Locate every uninfected red blood cell.
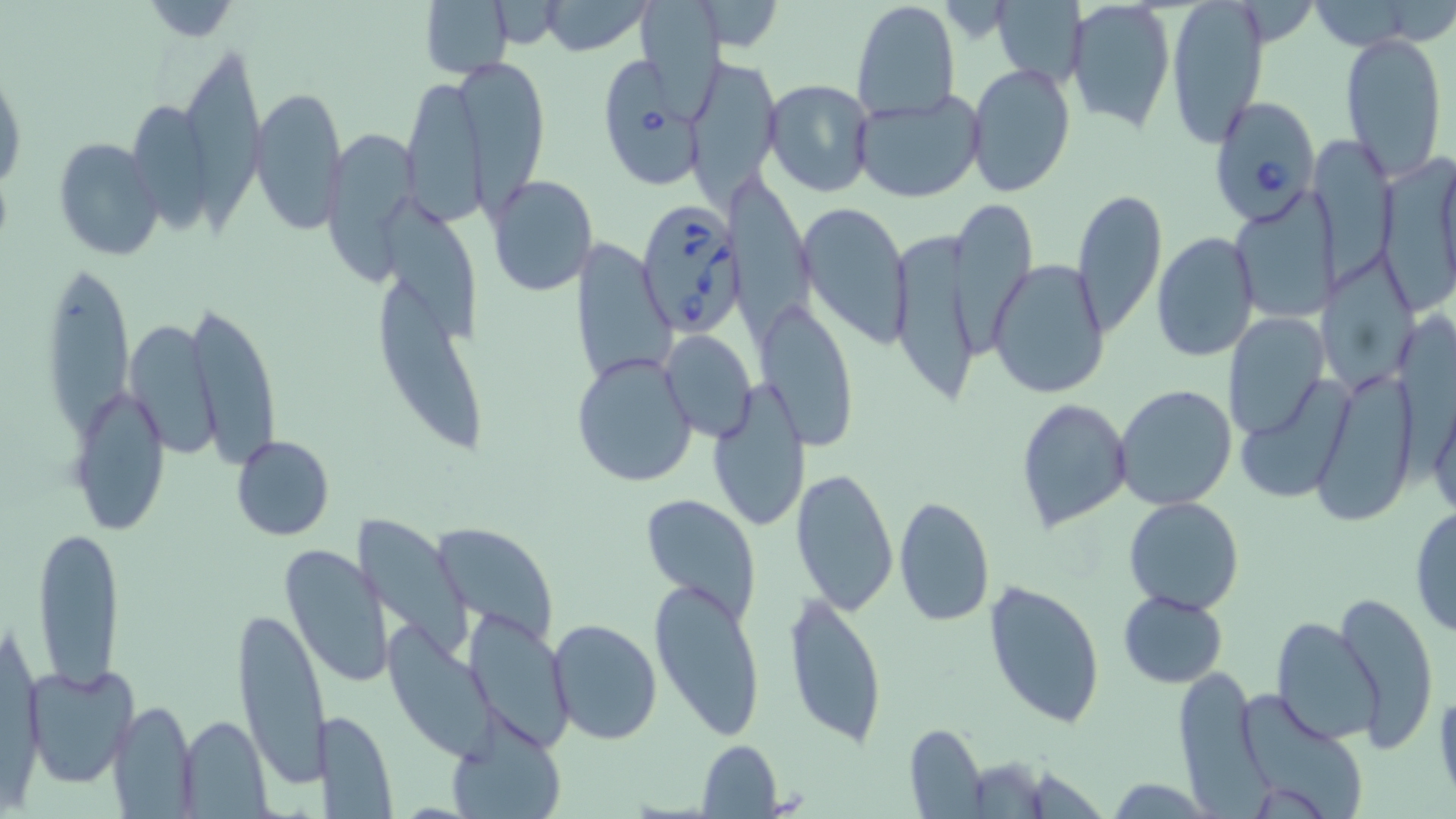
Approximate bounding boxes as named x1/y1/x2/y2 corners in pixels.
Uninfected red blood cells: (x1=420, y1=0, x2=514, y2=81), (x1=536, y1=0, x2=655, y2=56), (x1=850, y1=0, x2=960, y2=122), (x1=1166, y1=0, x2=1269, y2=148), (x1=1302, y1=0, x2=1431, y2=51), (x1=992, y1=2, x2=1086, y2=86), (x1=1066, y1=2, x2=1175, y2=135), (x1=137, y1=3, x2=245, y2=41), (x1=640, y1=3, x2=732, y2=124), (x1=1340, y1=31, x2=1448, y2=178), (x1=175, y1=39, x2=271, y2=224), (x1=686, y1=55, x2=781, y2=208), (x1=459, y1=56, x2=550, y2=207), (x1=965, y1=63, x2=1076, y2=198), (x1=0, y1=70, x2=25, y2=197), (x1=399, y1=74, x2=488, y2=228), (x1=763, y1=79, x2=875, y2=198), (x1=250, y1=85, x2=348, y2=235), (x1=850, y1=89, x2=984, y2=203), (x1=322, y1=127, x2=420, y2=281), (x1=1315, y1=133, x2=1396, y2=289), (x1=54, y1=138, x2=162, y2=260), (x1=1381, y1=155, x2=1456, y2=310), (x1=726, y1=165, x2=812, y2=340), (x1=485, y1=175, x2=598, y2=297), (x1=1070, y1=188, x2=1168, y2=339), (x1=1228, y1=191, x2=1339, y2=325), (x1=384, y1=192, x2=485, y2=348), (x1=951, y1=200, x2=1038, y2=357), (x1=796, y1=201, x2=912, y2=349), (x1=1152, y1=230, x2=1260, y2=363), (x1=889, y1=231, x2=984, y2=413), (x1=574, y1=239, x2=675, y2=388), (x1=1316, y1=251, x2=1422, y2=390), (x1=42, y1=253, x2=135, y2=454), (x1=988, y1=258, x2=1110, y2=401), (x1=379, y1=286, x2=486, y2=453), (x1=756, y1=298, x2=858, y2=451), (x1=184, y1=302, x2=280, y2=466), (x1=1222, y1=313, x2=1331, y2=442), (x1=121, y1=319, x2=223, y2=460), (x1=662, y1=329, x2=756, y2=444), (x1=572, y1=350, x2=697, y2=487), (x1=1314, y1=363, x2=1421, y2=525), (x1=1423, y1=371, x2=1456, y2=527), (x1=1235, y1=374, x2=1356, y2=504), (x1=707, y1=380, x2=812, y2=534), (x1=68, y1=383, x2=170, y2=537), (x1=1114, y1=384, x2=1238, y2=511), (x1=1016, y1=399, x2=1133, y2=533), (x1=230, y1=435, x2=335, y2=541), (x1=791, y1=466, x2=899, y2=617), (x1=640, y1=492, x2=762, y2=626), (x1=893, y1=495, x2=995, y2=628), (x1=1123, y1=496, x2=1244, y2=614), (x1=1409, y1=505, x2=1456, y2=638), (x1=34, y1=523, x2=125, y2=690), (x1=351, y1=525, x2=472, y2=662), (x1=433, y1=528, x2=560, y2=641), (x1=280, y1=543, x2=392, y2=689), (x1=649, y1=577, x2=765, y2=741), (x1=982, y1=579, x2=1104, y2=731), (x1=1334, y1=588, x2=1440, y2=751), (x1=1119, y1=589, x2=1229, y2=688), (x1=783, y1=591, x2=888, y2=750), (x1=231, y1=608, x2=331, y2=789), (x1=464, y1=609, x2=573, y2=754), (x1=1270, y1=616, x2=1382, y2=748), (x1=548, y1=617, x2=662, y2=744), (x1=382, y1=619, x2=504, y2=766), (x1=24, y1=663, x2=139, y2=788), (x1=1172, y1=669, x2=1266, y2=808), (x1=1432, y1=687, x2=1456, y2=812), (x1=1234, y1=689, x2=1372, y2=819), (x1=109, y1=700, x2=197, y2=815), (x1=319, y1=708, x2=397, y2=817), (x1=179, y1=715, x2=272, y2=815), (x1=445, y1=715, x2=568, y2=819), (x1=903, y1=723, x2=988, y2=817), (x1=697, y1=739, x2=783, y2=817).

Babesia divergens-infected red blood cell locations: (x1=601, y1=56, x2=701, y2=189), (x1=1206, y1=95, x2=1321, y2=226), (x1=636, y1=197, x2=743, y2=338). Slide-level diagnosis: Babesia divergens. Single field of view. Optical microscopy. May-Grünwald-Giemsa stain. Thin blood film. Image is 1456×819 pixels. Captured at 1000x magnification.